Classify this cell by malaria status.
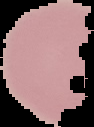

Uninfected.

Summary:
  - Image type: cell region segmented out of the field of view; surrounding area masked to black
  - Image size: 94×127 pixels
  - Preparation: thin blood film